Classify this cell by malaria status.
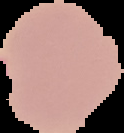

Uninfected.

image size = 124×133 pixels
preparation = thin blood smear
image type = segmented cell region with the area outside set to black